Classify this cell by malaria status.
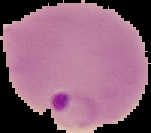

It is parasitized.

Summary:
  - Preparation: thin blood smear
  - Image size: 151×133 pixels
  - Image type: segmented cell region with the area outside set to black